Point out each Plasmodium parasite.
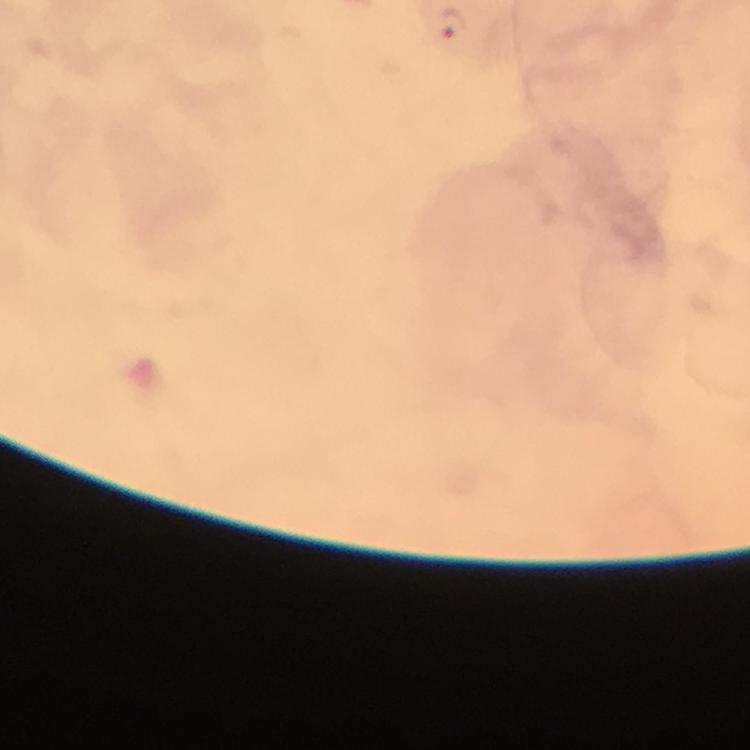

Approximate centers as (x, y) in pixels.
Plasmodium parasites: (451, 23).

Photographed through the microscope with a smartphone camera. Image is 750×750 pixels. Giemsa-stained preparation. Thick smear. A crop from one field of view. Immersion oil applied. From a diagnostic examination for malaria. At 100x magnification.